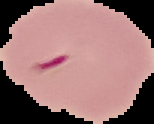

result = malaria parasites detected
preparation = thin blood smear
image size = 154×124 pixels
image type = segmented cell region on a black background